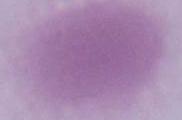

magnification = 1000x
modality = photomicrograph
identification = red blood cell